Name the parasite shown.
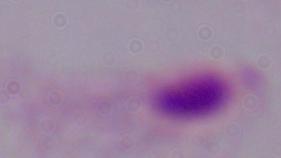
This is a trichomonad.

Photomicrograph. 1000x magnification.